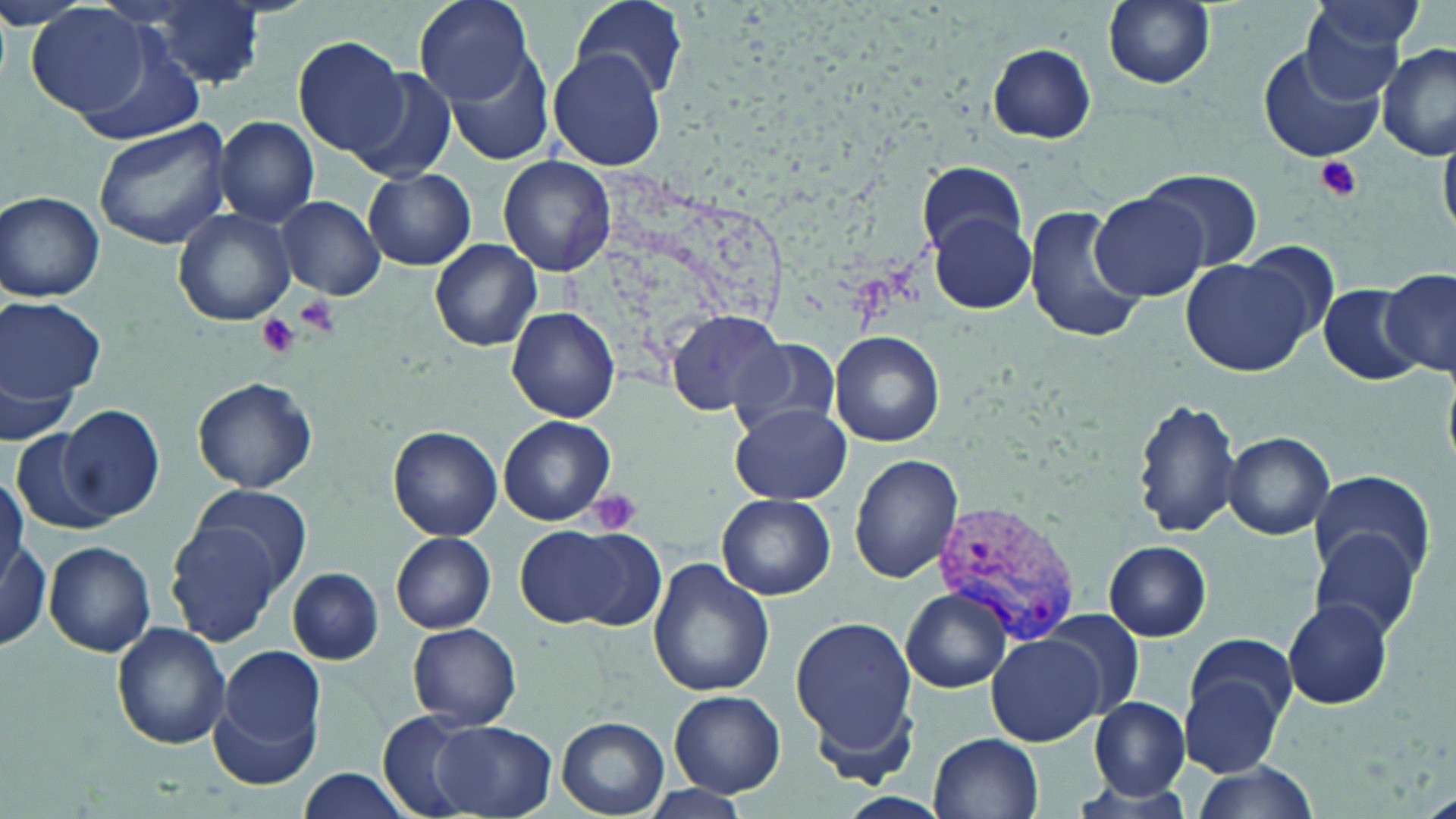

Summary:
  - Coordinate format: approximate bounding boxes as [x1, y1, x2, y2] in pixels
  - Uninfected red blood cell locations: [413, 0, 533, 107], [571, 0, 689, 100], [1102, 0, 1217, 89], [1294, 0, 1425, 97], [134, 2, 268, 89], [27, 4, 153, 118], [69, 29, 206, 144], [293, 36, 409, 155], [1256, 42, 1388, 164], [1377, 42, 1455, 159], [988, 43, 1097, 144], [441, 46, 554, 166], [550, 47, 667, 173], [352, 70, 459, 183], [215, 116, 319, 225], [94, 120, 232, 250], [500, 156, 616, 275], [917, 162, 1027, 253], [1137, 168, 1264, 272], [363, 169, 475, 270], [0, 191, 104, 302], [1090, 192, 1209, 301], [277, 196, 384, 300], [1022, 205, 1143, 345], [174, 209, 295, 326], [928, 212, 1035, 312], [429, 238, 543, 350], [1242, 240, 1342, 339], [1179, 257, 1316, 376], [1381, 267, 1456, 378], [1318, 284, 1424, 384], [0, 297, 105, 402], [508, 307, 620, 424], [665, 311, 791, 418], [828, 330, 946, 445], [727, 336, 843, 438], [0, 365, 83, 446], [194, 378, 316, 493], [1134, 397, 1241, 540], [60, 404, 166, 521], [733, 404, 852, 505], [499, 416, 614, 526], [389, 426, 501, 541], [11, 431, 110, 535], [1223, 431, 1335, 538], [849, 454, 963, 582], [1310, 473, 1434, 579], [186, 482, 313, 592], [717, 494, 835, 600], [166, 517, 284, 647], [518, 525, 662, 632], [0, 530, 49, 652], [1308, 531, 1422, 639], [392, 533, 495, 634], [1103, 541, 1211, 641], [44, 542, 155, 655], [649, 559, 775, 697], [287, 567, 383, 664], [903, 590, 1012, 693], [1283, 599, 1392, 710], [1045, 609, 1147, 718], [789, 616, 917, 766], [112, 622, 230, 750], [408, 622, 522, 728], [1185, 633, 1299, 735], [987, 634, 1104, 746], [215, 647, 327, 769], [1180, 666, 1289, 775], [668, 688, 785, 797], [1089, 696, 1191, 799], [377, 711, 479, 815], [558, 718, 668, 816], [429, 721, 556, 817], [929, 732, 1043, 819], [1186, 763, 1319, 818], [295, 769, 409, 818], [639, 783, 752, 819]
  - Platelet locations: [1314, 156, 1363, 201], [290, 295, 340, 335], [254, 313, 301, 359], [586, 487, 644, 537]
  - Plasmodium vivax-infected red blood cell locations: [937, 506, 1075, 646]
  - Slide-level diagnosis: Plasmodium vivax
  - Stain: May-Grünwald-Giemsa
  - Image size: 1456×819 pixels
  - Preparation: thin blood smear
  - Modality: light microscopy
  - Magnification: 1000x
  - Field of view: single